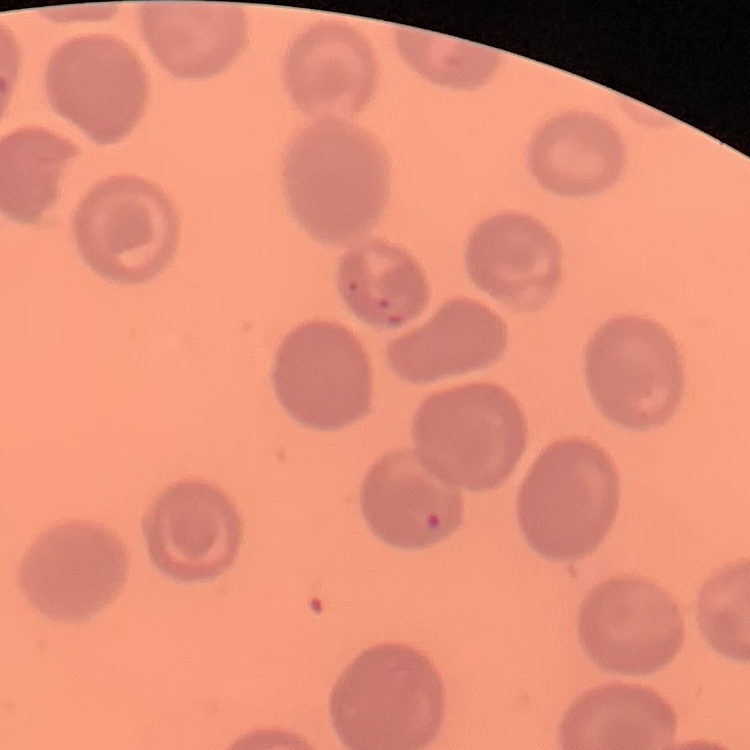

red blood cell morphology = no rouleaux formation
image type = one tile cut from a larger photomicrograph
stain = Field's or Giemsa
preparation = thin blood film